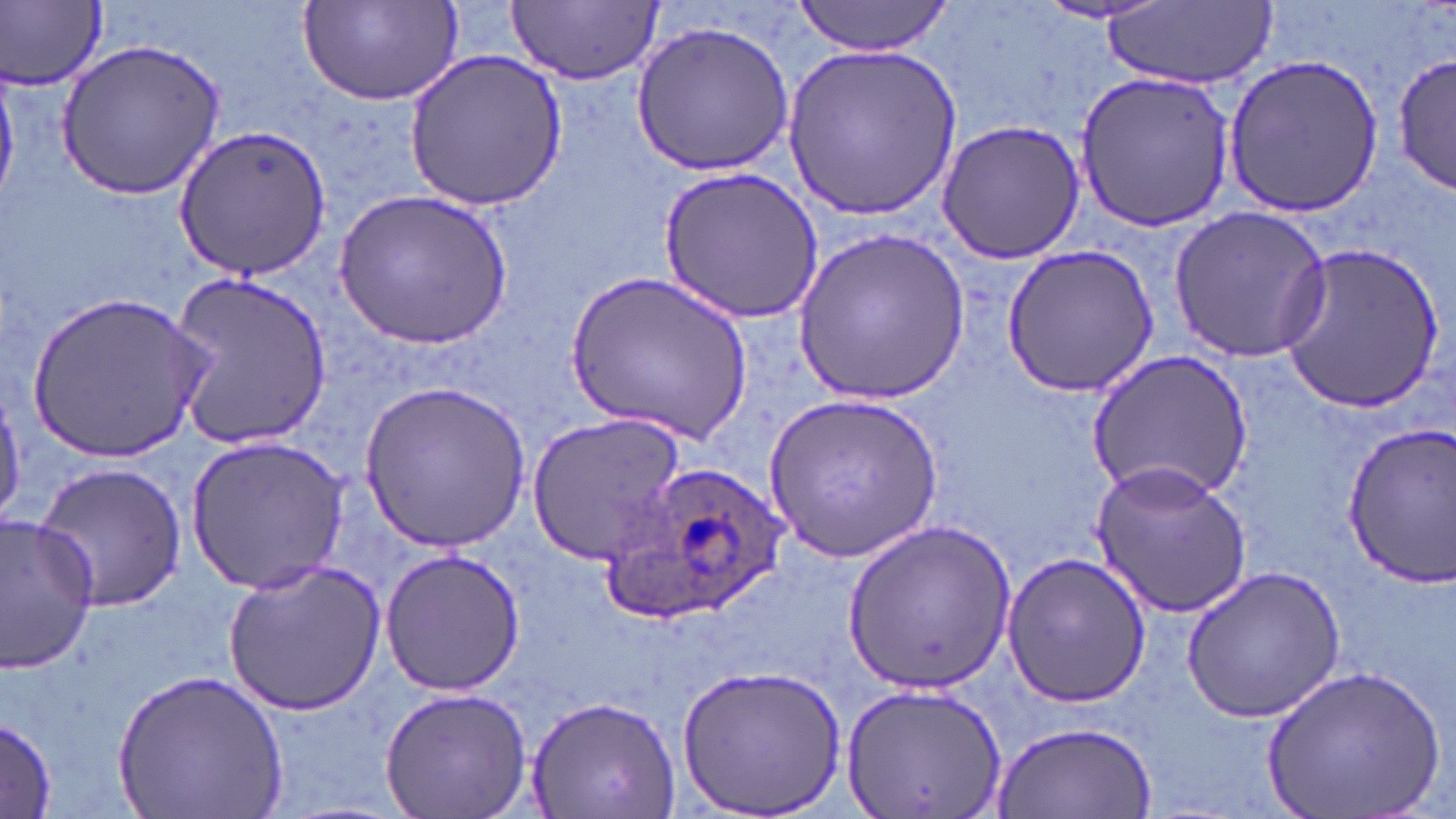

Approximate bounding boxes as (x1, y1, x2, y2) in pixels. Uninfected red blood cell locations: (792, 0, 957, 58), (1032, 0, 1176, 26), (297, 1, 464, 108), (507, 1, 662, 85), (3, 2, 107, 90), (1105, 3, 1273, 89), (631, 20, 796, 174), (57, 37, 227, 199), (783, 43, 960, 223), (1391, 47, 1454, 200), (404, 50, 567, 211), (1220, 53, 1385, 219), (1075, 70, 1237, 234), (936, 119, 1085, 265), (172, 124, 334, 282), (660, 167, 823, 321), (336, 188, 511, 349), (1168, 207, 1331, 362), (791, 228, 971, 406), (1274, 240, 1445, 410), (1003, 244, 1162, 396), (567, 265, 752, 447), (168, 271, 334, 454), (27, 289, 211, 462), (1084, 348, 1254, 501), (359, 379, 531, 553), (765, 391, 943, 561), (526, 412, 688, 562), (1336, 424, 1456, 587), (185, 436, 348, 594), (35, 460, 188, 614), (1089, 460, 1251, 617), (0, 512, 101, 675), (843, 518, 1014, 693), (379, 548, 525, 698), (999, 550, 1151, 710), (223, 560, 386, 714), (1181, 566, 1346, 723), (676, 663, 846, 817), (1265, 664, 1443, 819), (112, 667, 290, 819), (841, 685, 1008, 815), (378, 686, 531, 818), (525, 693, 682, 816), (0, 715, 60, 818), (993, 722, 1158, 818). Plasmodium ovale-infected red blood cell locations: (605, 463, 793, 623). Slide-level diagnosis: Plasmodium ovale. One field of a larger specimen. Image is 1456×819 pixels. 1000x magnification. Thin blood smear. Light microscopy. May-Grünwald-Giemsa-stained preparation.